Report the malaria status of this cell.
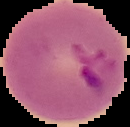

It is parasitized.

preparation = thin blood film
image size = 130×127 pixels
image type = cell region segmented out of the field of view; surrounding area masked to black